Identify the parasite.
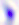

This is Toxoplasma gondii.

Summary:
  - Magnification: 400x
  - Modality: micrograph